Give the extent of all Plasmodium ovale-infected red blood cells.
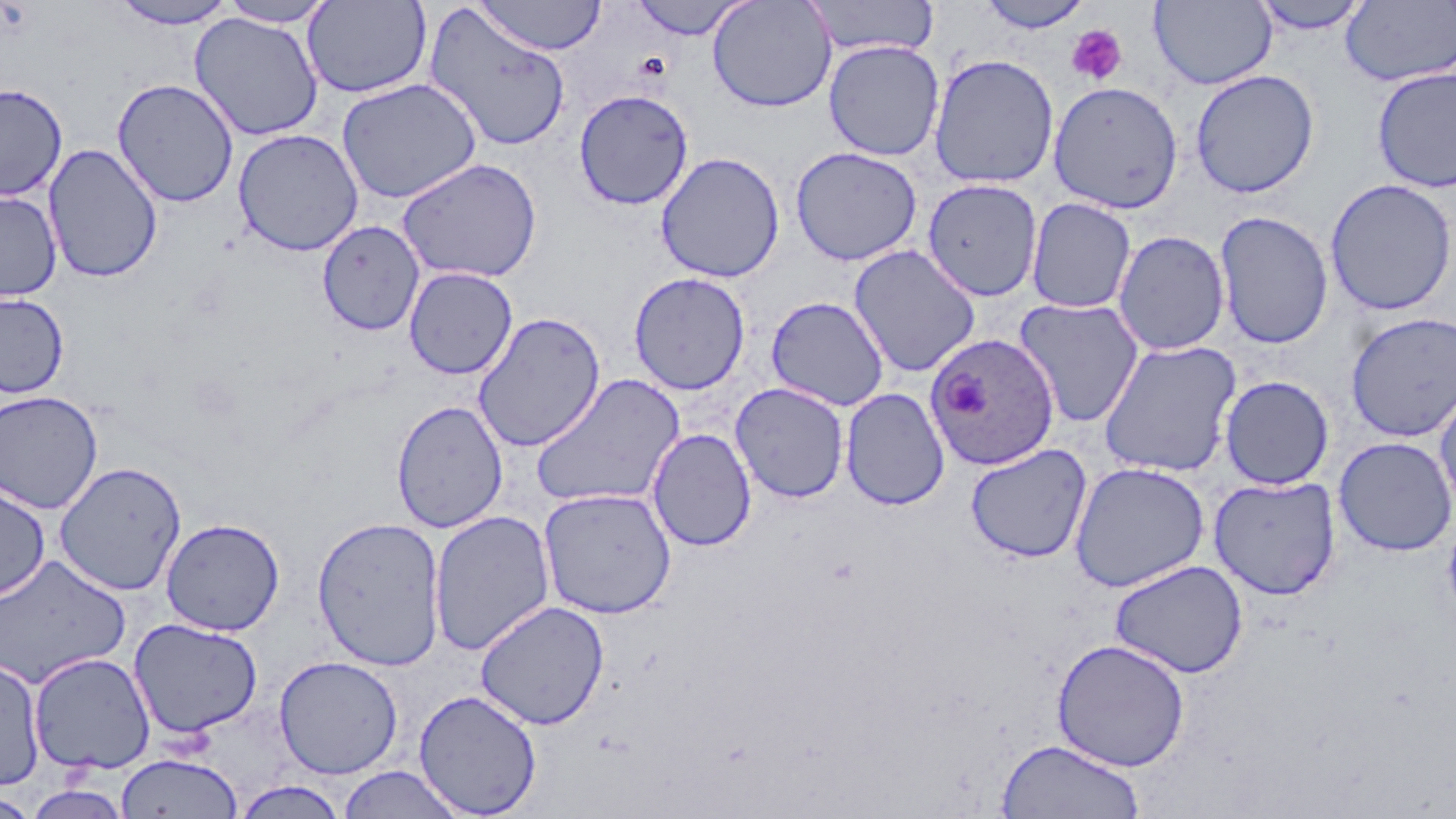

Approximate bounding boxes as (x1, y1, x2, y2) in pixels.
Plasmodium ovale-infected red blood cells: (924, 332, 1060, 470).

Summary:
  - Platelet locations: (1065, 24, 1128, 85)
  - Uninfected red blood cell locations: (475, 0, 607, 55), (625, 0, 754, 40), (707, 0, 837, 113), (802, 0, 941, 58), (974, 0, 1095, 34), (108, 1, 241, 29), (217, 1, 336, 27), (302, 1, 433, 99), (1149, 1, 1277, 90), (1249, 1, 1373, 35), (1341, 1, 1456, 87), (421, 4, 572, 153), (188, 13, 325, 141), (824, 40, 944, 161), (928, 53, 1060, 189), (1371, 66, 1456, 194), (1189, 69, 1320, 198), (112, 78, 240, 208), (336, 78, 483, 204), (1047, 80, 1184, 214), (0, 82, 68, 201), (573, 89, 694, 210), (232, 128, 364, 256), (43, 142, 163, 284), (790, 146, 923, 266), (655, 151, 785, 283), (397, 157, 542, 284), (922, 178, 1043, 301), (1324, 179, 1456, 316), (0, 190, 62, 303), (1025, 197, 1136, 314), (1214, 211, 1334, 349), (316, 220, 425, 337), (1112, 230, 1231, 356), (848, 244, 981, 377), (404, 266, 518, 379), (628, 272, 750, 395), (0, 292, 69, 399), (765, 296, 889, 411), (1013, 297, 1144, 428), (472, 311, 606, 452), (1345, 312, 1456, 442), (1098, 339, 1241, 477), (531, 373, 685, 511), (1219, 375, 1334, 490), (1433, 379, 1456, 517), (730, 382, 850, 503), (840, 387, 951, 511), (0, 390, 104, 514), (391, 399, 508, 533), (647, 428, 757, 552), (1333, 436, 1456, 556), (965, 443, 1092, 563), (54, 461, 187, 596), (1068, 461, 1210, 593), (1208, 476, 1340, 600), (0, 480, 51, 602), (537, 487, 677, 619), (1442, 506, 1456, 632), (428, 509, 555, 656), (311, 516, 447, 671), (160, 518, 285, 636), (1, 554, 130, 690), (1109, 559, 1248, 679), (474, 600, 610, 730), (129, 617, 264, 738), (1051, 638, 1190, 771), (28, 652, 156, 774), (0, 655, 46, 791), (274, 655, 403, 779), (413, 689, 543, 817), (996, 738, 1145, 818), (115, 752, 243, 819), (337, 766, 466, 818), (231, 781, 350, 819), (21, 783, 133, 819), (0, 792, 42, 817)
  - Slide-level diagnosis: Plasmodium ovale
  - Preparation: thin blood film
  - Stain: May-Grünwald-Giemsa
  - Field of view: single
  - Magnification: 1000x
  - Image size: 1456×819 pixels
  - Modality: optical microscopy